Give the position of every leukocyte visible.
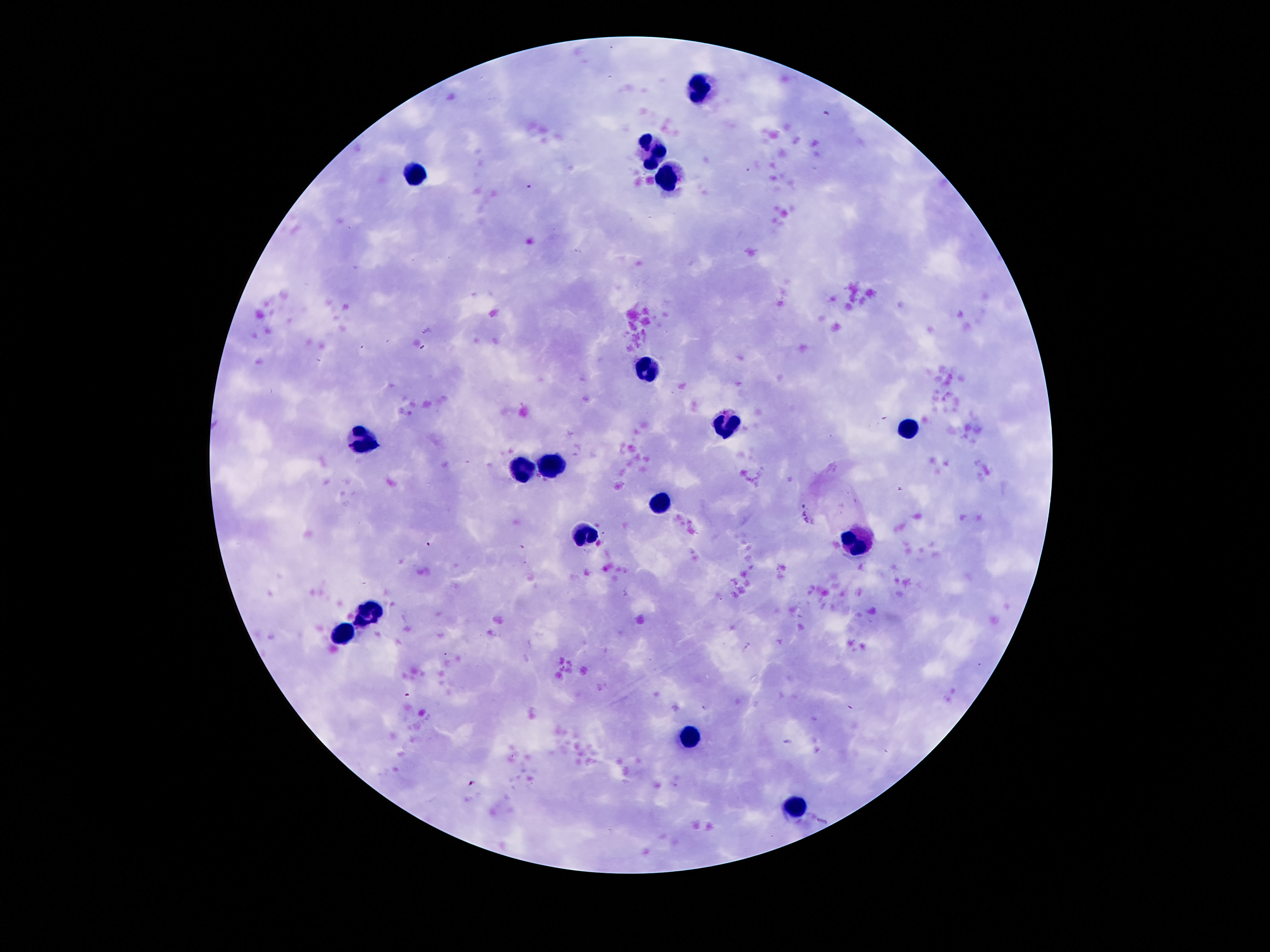

Approximate centers as {x, y} in pixels.
Leukocytes: {702, 87}, {651, 152}, {416, 175}, {666, 179}, {649, 370}, {725, 421}, {908, 427}, {366, 437}, {550, 465}, {521, 469}, {662, 503}, {584, 534}, {857, 545}, {368, 616}, {345, 635}, {689, 736}, {792, 807}.

Summary:
  - Preparation: thick blood film
  - Image size: 1270×952 pixels
  - Capture: smartphone camera through the microscope eyepiece
  - Field of view: single
  - Magnification: 100x
  - Stain: Giemsa
  - Patient malaria status: uninfected